Locate every blood parasite and identify its species.
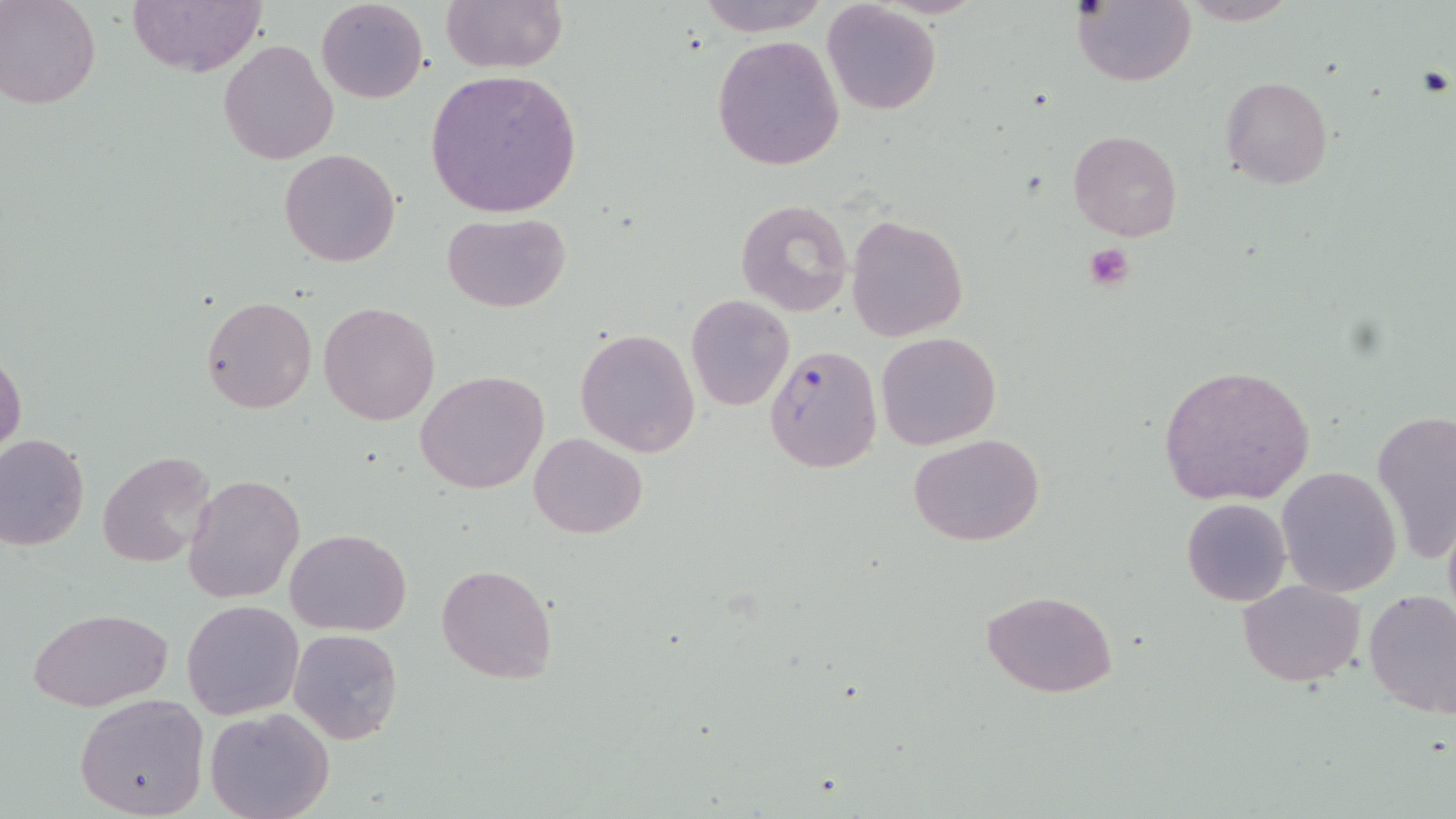

Approximate bounding boxes as named x1/y1/x2/y2 corners in pixels.
Plasmodium falciparum-infected red blood cells: (x1=764, y1=344, x2=882, y2=473).
No Plasmodium ovale, Plasmodium malariae, Plasmodium vivax, Babesia divergens, or Trypanosoma brucei observed.

slide-level diagnosis = Plasmodium falciparum
image size = 1456×819 pixels
stain = May-Grünwald-Giemsa
modality = light microscopy
field of view = single
uninfected red blood cell locations = approximate bounding boxes as named x1/y1/x2/y2 corners in pixels: (x1=2, y1=0, x2=100, y2=109), (x1=315, y1=0, x2=429, y2=103), (x1=439, y1=0, x2=568, y2=74), (x1=695, y1=0, x2=831, y2=35), (x1=1075, y1=0, x2=1196, y2=86), (x1=1182, y1=0, x2=1296, y2=25), (x1=126, y1=2, x2=266, y2=77), (x1=822, y1=3, x2=942, y2=115), (x1=712, y1=35, x2=844, y2=172), (x1=218, y1=39, x2=339, y2=166), (x1=424, y1=68, x2=583, y2=219), (x1=1220, y1=75, x2=1333, y2=190), (x1=1068, y1=130, x2=1182, y2=242), (x1=278, y1=149, x2=401, y2=266), (x1=735, y1=198, x2=852, y2=316), (x1=442, y1=211, x2=569, y2=311), (x1=844, y1=213, x2=968, y2=342), (x1=200, y1=294, x2=316, y2=414), (x1=685, y1=294, x2=795, y2=411), (x1=319, y1=301, x2=439, y2=426), (x1=575, y1=328, x2=701, y2=457), (x1=876, y1=331, x2=1002, y2=449), (x1=0, y1=352, x2=26, y2=458), (x1=1157, y1=364, x2=1316, y2=506), (x1=415, y1=370, x2=549, y2=495), (x1=1373, y1=410, x2=1456, y2=566), (x1=909, y1=432, x2=1045, y2=547), (x1=529, y1=433, x2=647, y2=540), (x1=0, y1=434, x2=91, y2=551), (x1=95, y1=450, x2=217, y2=566), (x1=1276, y1=467, x2=1400, y2=596), (x1=185, y1=473, x2=305, y2=605), (x1=1181, y1=498, x2=1291, y2=606), (x1=1442, y1=509, x2=1456, y2=636), (x1=286, y1=529, x2=411, y2=636), (x1=437, y1=564, x2=557, y2=683), (x1=1239, y1=580, x2=1366, y2=687), (x1=1364, y1=587, x2=1456, y2=720), (x1=981, y1=589, x2=1119, y2=696), (x1=182, y1=601, x2=302, y2=720), (x1=29, y1=608, x2=172, y2=711), (x1=288, y1=627, x2=403, y2=746), (x1=72, y1=693, x2=209, y2=818), (x1=205, y1=706, x2=333, y2=819)
preparation = thin blood smear
platelet locations = approximate bounding boxes as named x1/y1/x2/y2 corners in pixels: (x1=1082, y1=242, x2=1135, y2=292)
magnification = 1000x